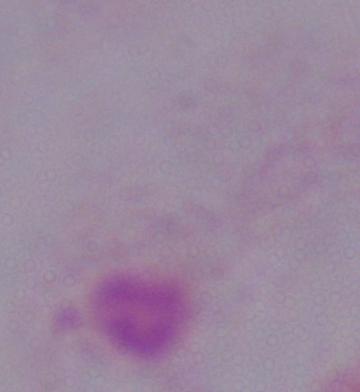

Summary:
  - Modality: micrograph
  - Magnification: 1000x
  - Identification: trichomonad